Report the malaria status of this cell.
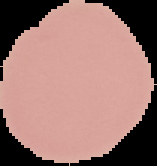

It is uninfected.

Summary:
  - Preparation: thin blood film
  - Image type: segmented cell region on a black background
  - Image size: 157×166 pixels